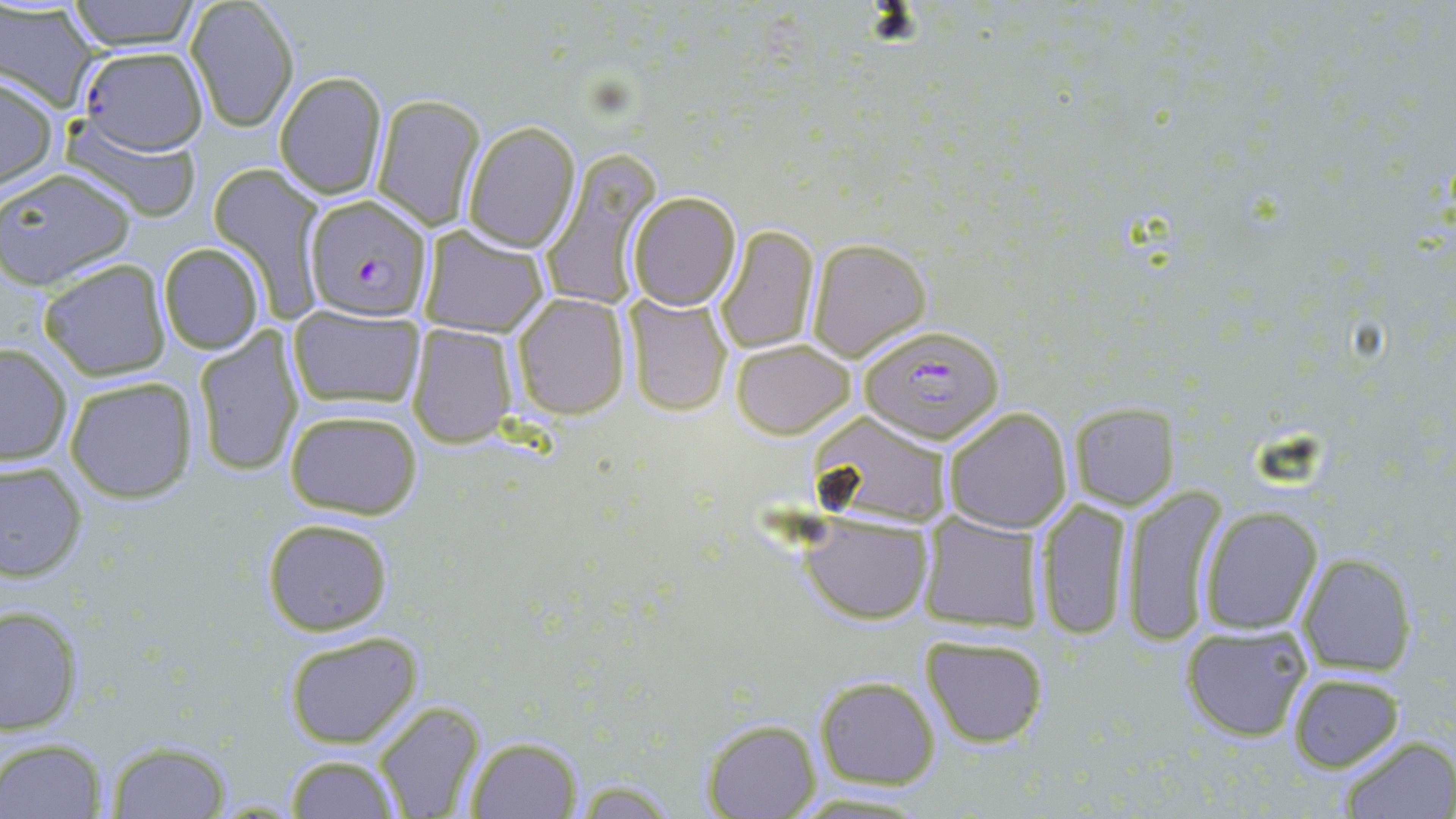
Approximate bounding boxes as (x1, y1, x2, y2) in pixels. Uninfected red blood cell locations: (64, 0, 202, 51), (184, 0, 299, 132), (0, 3, 98, 110), (77, 46, 208, 155), (273, 71, 389, 200), (0, 74, 58, 195), (372, 94, 486, 230), (58, 118, 203, 221), (461, 121, 581, 252), (542, 147, 663, 313), (208, 163, 326, 317), (0, 167, 135, 287), (627, 191, 742, 310), (715, 223, 820, 354), (417, 225, 549, 337), (805, 238, 932, 362), (158, 243, 265, 356), (40, 260, 170, 382), (512, 293, 631, 421), (622, 293, 733, 417), (288, 306, 425, 413), (405, 323, 519, 449), (191, 328, 305, 478), (730, 339, 855, 438), (0, 343, 74, 465), (65, 378, 198, 501), (1066, 402, 1181, 510), (942, 406, 1073, 533), (282, 407, 423, 521), (810, 413, 952, 525), (0, 460, 87, 581), (1121, 486, 1231, 646), (1033, 496, 1136, 640), (1198, 507, 1323, 635), (918, 510, 1043, 634), (802, 513, 932, 624), (260, 517, 395, 637), (1294, 554, 1419, 678), (0, 602, 83, 738), (1180, 623, 1313, 741), (282, 631, 424, 748), (919, 633, 1050, 749), (1287, 672, 1404, 771), (814, 675, 941, 789), (373, 700, 485, 819), (698, 717, 822, 819), (1335, 734, 1455, 818), (464, 735, 584, 817), (1, 737, 108, 818), (101, 742, 233, 816), (283, 753, 402, 818), (786, 788, 939, 817). Plasmodium falciparum-infected red blood cell locations: (302, 194, 433, 322), (855, 324, 1006, 446). Slide-level diagnosis: Plasmodium falciparum. May-Grünwald-Giemsa stain. 1000x magnification. Optical microscopy. One field of a larger specimen. Image is 1456×819 pixels. Thin blood smear.